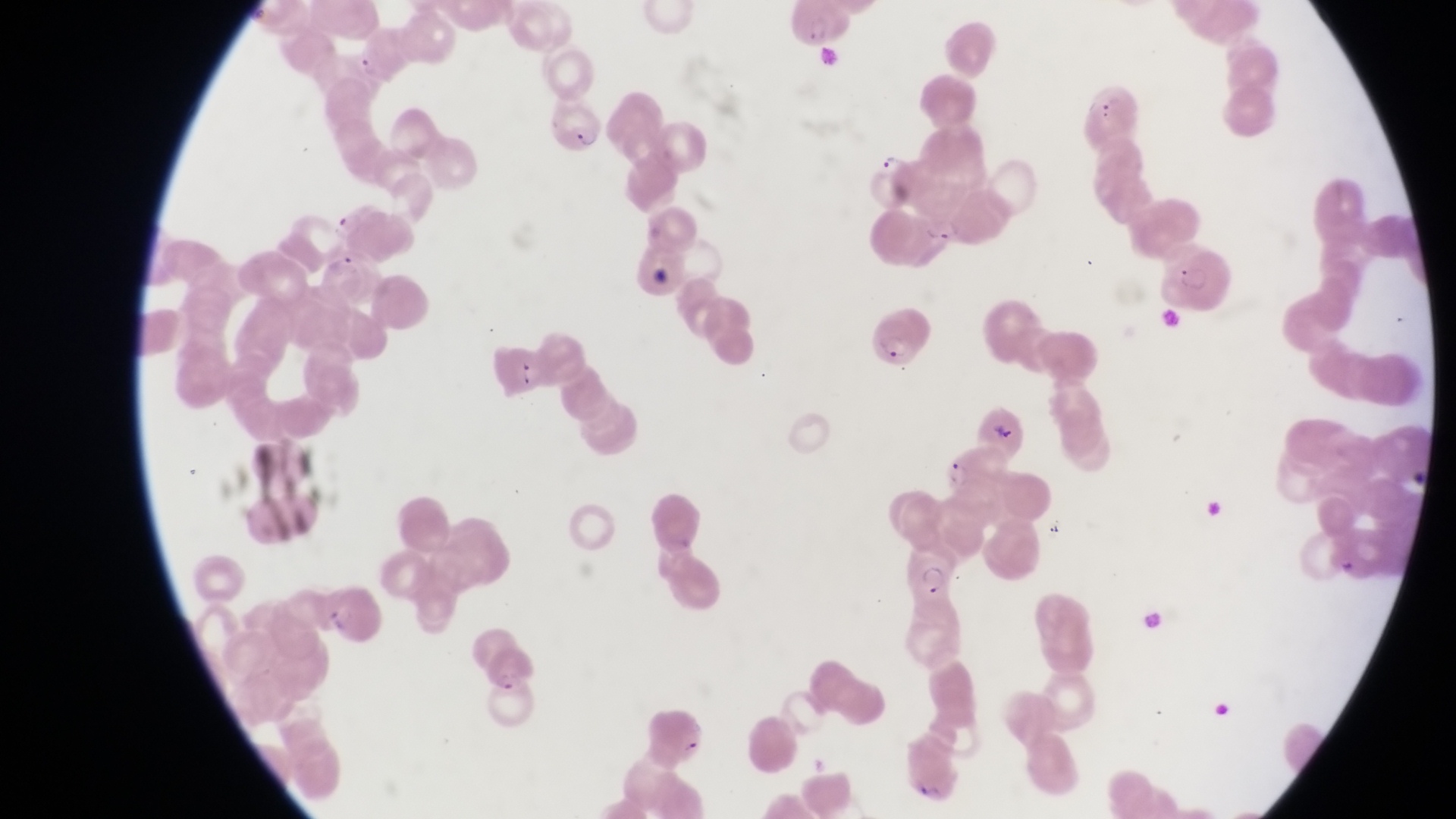
{
  "trophozoite_locations": "approximate bounding boxes as [left, top, right, bottom] in pixels: [875, 148, 899, 172]",
  "parasitised_red_blood_cell_locations": "approximate bounding boxes as [left, top, right, bottom] in pixels: [786, 2, 853, 51], [346, 42, 399, 92], [1081, 77, 1140, 144], [552, 102, 604, 157], [334, 208, 408, 254], [1162, 251, 1234, 311], [865, 306, 938, 375], [945, 452, 1000, 502], [902, 541, 966, 601]",
  "artifact_platelet_like_body_stain_precipitate_or_debris_locations": "approximate bounding boxes as [left, top, right, bottom] in pixels: [1158, 304, 1181, 334], [1337, 555, 1358, 581]",
  "field_of_view": "single",
  "magnification": "1000x",
  "image_size": "1456×819 pixels",
  "capture": "smartphone photograph through the eyepiece of an Olympus CX-23 microscope",
  "preparation": "thin blood smear",
  "country": "Uganda"
}